State which parasite is depicted.
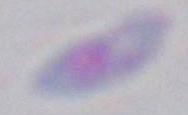

This is Toxoplasma gondii.

Summary:
  - Magnification: 1000x
  - Modality: micrograph